Classify this cell by malaria status.
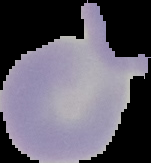
It is uninfected.

Image is 151×163 pixels. Cell region segmented out of the field of view; the surrounding area is masked to black. From a thin blood film.